Describe the morphology of the erythrocytes.
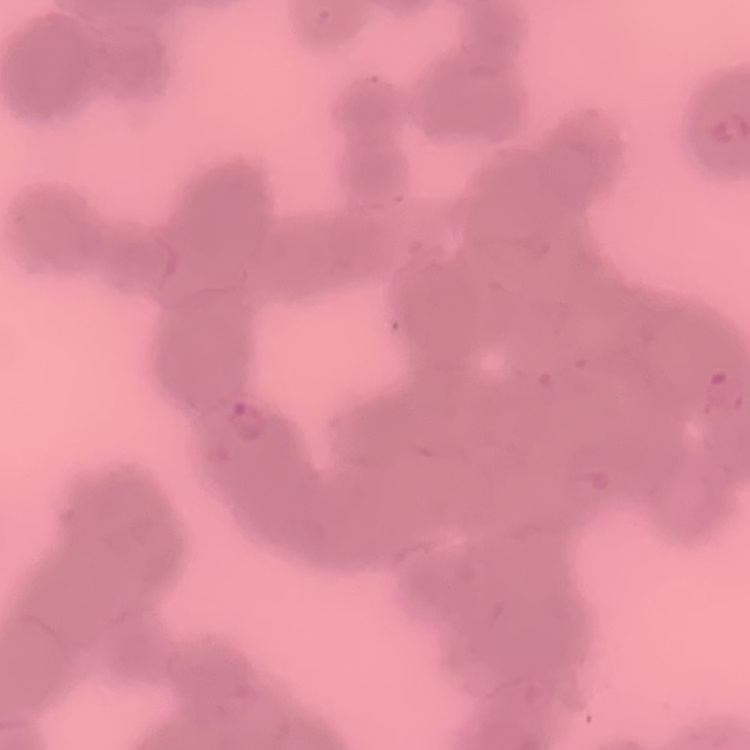
They show rouleaux formation.

Summary:
  - Stain: Field's or Giemsa
  - Preparation: thin blood smear
  - Image type: one tile cut from a larger photomicrograph